Assess the morphology of the erythrocytes.
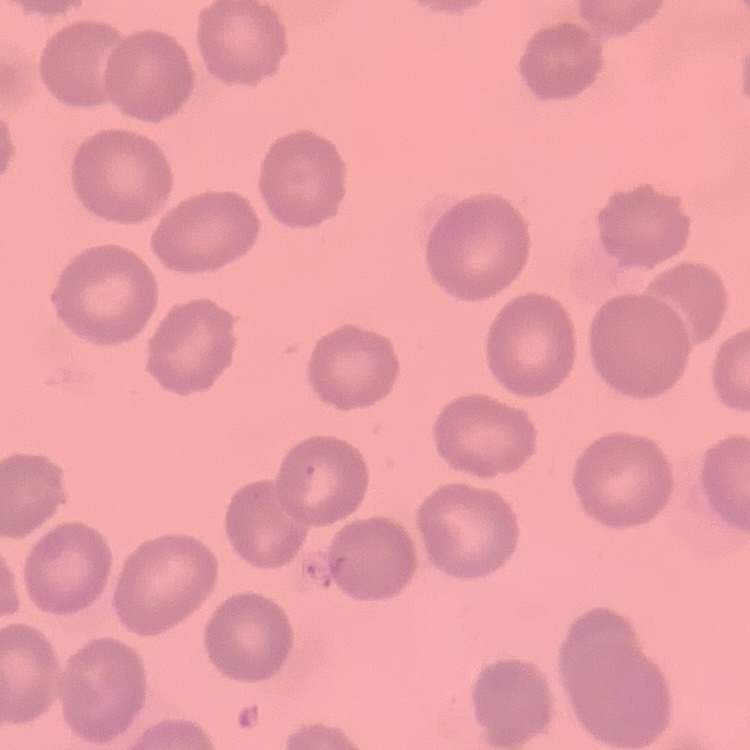

No rouleaux formation.

image_type: one tile cut from a larger photomicrograph
stain: Field's or Giemsa
preparation: thin blood film